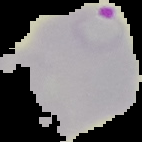
image type = cell region segmented out of the field of view; surrounding area masked to black
malaria status = parasitized
image size = 142×142 pixels
preparation = thin blood smear